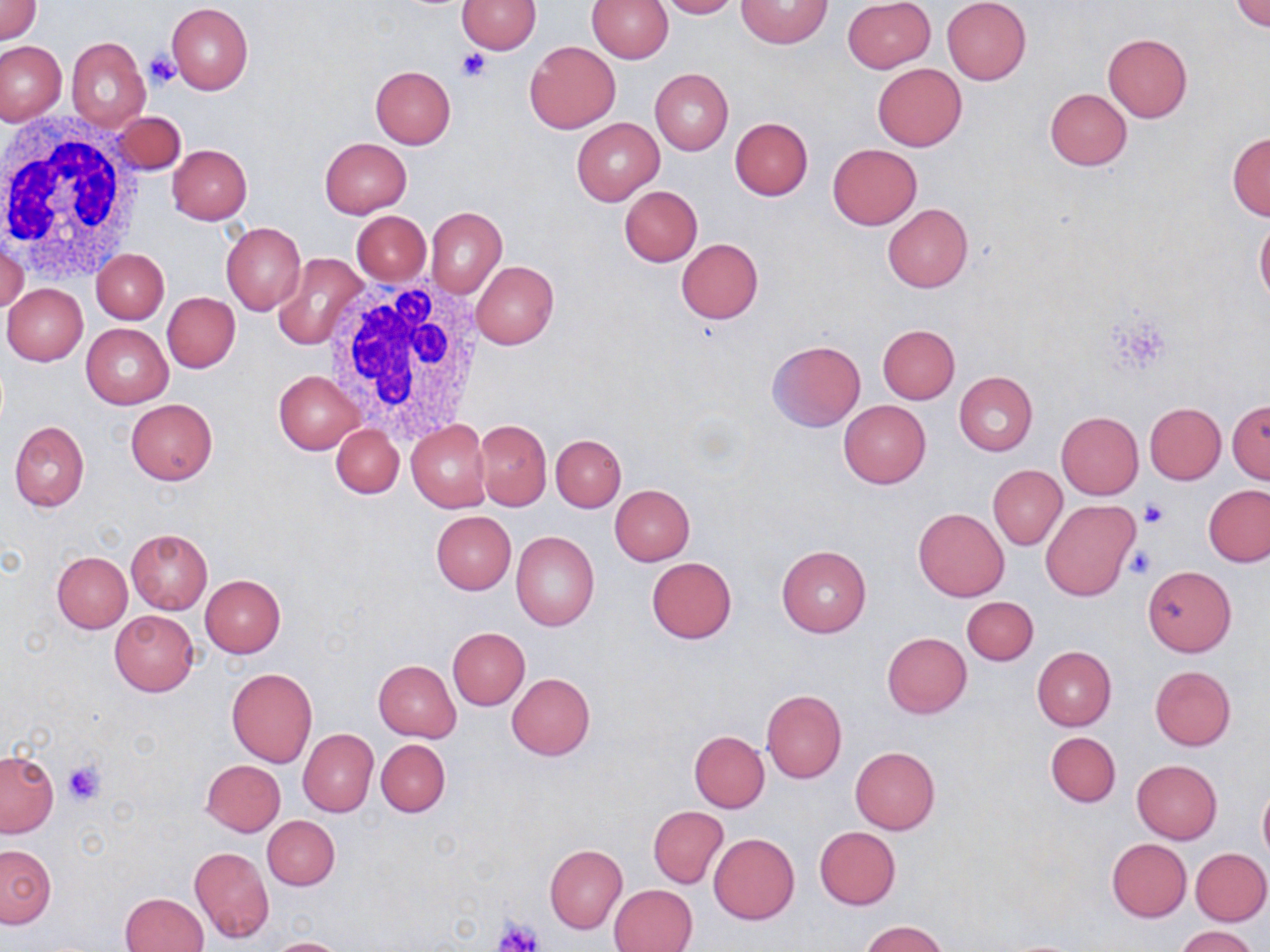
Summary:
  - Coordinate format: approximate bounding boxes as named x1/y1/x2/y2 corners in pixels
  - Uninfected red blood cell locations: (x1=0, y1=0, x2=41, y2=42), (x1=457, y1=0, x2=541, y2=54), (x1=587, y1=0, x2=673, y2=63), (x1=657, y1=0, x2=738, y2=18), (x1=736, y1=0, x2=832, y2=48), (x1=843, y1=0, x2=935, y2=72), (x1=943, y1=0, x2=1032, y2=85), (x1=1233, y1=0, x2=1270, y2=33), (x1=167, y1=2, x2=253, y2=94), (x1=1103, y1=32, x2=1192, y2=121), (x1=67, y1=37, x2=149, y2=130), (x1=0, y1=40, x2=65, y2=124), (x1=525, y1=40, x2=620, y2=134), (x1=873, y1=63, x2=967, y2=150), (x1=371, y1=66, x2=456, y2=148), (x1=650, y1=68, x2=733, y2=155), (x1=1045, y1=89, x2=1131, y2=171), (x1=113, y1=111, x2=185, y2=175), (x1=572, y1=117, x2=664, y2=205), (x1=730, y1=117, x2=813, y2=199), (x1=1227, y1=133, x2=1270, y2=220), (x1=320, y1=137, x2=411, y2=217), (x1=828, y1=143, x2=922, y2=230), (x1=169, y1=145, x2=252, y2=224), (x1=621, y1=186, x2=702, y2=266), (x1=882, y1=203, x2=973, y2=293), (x1=425, y1=206, x2=507, y2=298), (x1=353, y1=211, x2=430, y2=285), (x1=1255, y1=215, x2=1270, y2=304), (x1=222, y1=222, x2=305, y2=316), (x1=1, y1=237, x2=29, y2=317), (x1=676, y1=238, x2=763, y2=323), (x1=93, y1=249, x2=169, y2=323), (x1=274, y1=252, x2=368, y2=351), (x1=471, y1=260, x2=558, y2=349), (x1=3, y1=283, x2=87, y2=366), (x1=162, y1=292, x2=240, y2=373), (x1=82, y1=324, x2=172, y2=408), (x1=877, y1=324, x2=960, y2=404), (x1=767, y1=340, x2=866, y2=431), (x1=274, y1=370, x2=365, y2=453), (x1=954, y1=371, x2=1037, y2=455), (x1=126, y1=400, x2=217, y2=484), (x1=838, y1=401, x2=931, y2=488), (x1=1228, y1=401, x2=1270, y2=484), (x1=1145, y1=403, x2=1225, y2=484), (x1=1056, y1=412, x2=1143, y2=499), (x1=474, y1=419, x2=551, y2=510), (x1=10, y1=420, x2=89, y2=512), (x1=407, y1=420, x2=490, y2=511), (x1=331, y1=423, x2=404, y2=499), (x1=552, y1=434, x2=626, y2=511), (x1=989, y1=466, x2=1066, y2=549), (x1=609, y1=484, x2=695, y2=565), (x1=1203, y1=485, x2=1270, y2=566), (x1=1042, y1=499, x2=1140, y2=602), (x1=913, y1=508, x2=1009, y2=602), (x1=431, y1=511, x2=515, y2=594), (x1=126, y1=529, x2=212, y2=613), (x1=511, y1=531, x2=601, y2=631), (x1=776, y1=545, x2=871, y2=637), (x1=52, y1=551, x2=131, y2=632), (x1=646, y1=557, x2=738, y2=643), (x1=1144, y1=564, x2=1236, y2=655), (x1=200, y1=574, x2=286, y2=657), (x1=963, y1=596, x2=1038, y2=664), (x1=109, y1=611, x2=199, y2=695), (x1=448, y1=627, x2=529, y2=709), (x1=881, y1=632, x2=971, y2=717), (x1=1032, y1=646, x2=1116, y2=730), (x1=373, y1=660, x2=460, y2=742), (x1=1150, y1=666, x2=1237, y2=750), (x1=227, y1=667, x2=317, y2=767), (x1=506, y1=673, x2=595, y2=761), (x1=761, y1=689, x2=847, y2=782), (x1=298, y1=729, x2=378, y2=817), (x1=689, y1=731, x2=770, y2=813), (x1=1045, y1=731, x2=1119, y2=807), (x1=376, y1=739, x2=449, y2=817), (x1=850, y1=746, x2=940, y2=833), (x1=0, y1=750, x2=57, y2=837), (x1=201, y1=759, x2=285, y2=835), (x1=1132, y1=760, x2=1222, y2=844), (x1=1258, y1=780, x2=1270, y2=866), (x1=648, y1=806, x2=727, y2=888), (x1=262, y1=816, x2=339, y2=890), (x1=814, y1=826, x2=901, y2=909), (x1=709, y1=832, x2=799, y2=924), (x1=1106, y1=838, x2=1191, y2=921), (x1=0, y1=845, x2=55, y2=927), (x1=545, y1=845, x2=626, y2=932), (x1=190, y1=846, x2=274, y2=942), (x1=1190, y1=847, x2=1270, y2=924), (x1=611, y1=884, x2=697, y2=952), (x1=120, y1=892, x2=208, y2=952), (x1=862, y1=921, x2=947, y2=952), (x1=1175, y1=926, x2=1258, y2=952), (x1=264, y1=937, x2=352, y2=952)
  - Platelet locations: (x1=456, y1=46, x2=490, y2=82), (x1=144, y1=53, x2=180, y2=90), (x1=1141, y1=499, x2=1170, y2=529), (x1=1124, y1=547, x2=1157, y2=579), (x1=64, y1=759, x2=104, y2=806), (x1=497, y1=917, x2=544, y2=950)
  - White blood cell locations: (x1=0, y1=118, x2=149, y2=283), (x1=321, y1=275, x2=491, y2=444)
  - Slide-level diagnosis: no evidence of blood parasites
  - Modality: optical microscopy
  - Preparation: thin blood smear
  - Magnification: 1000x
  - Field of view: one of a larger specimen
  - Image size: 1270×952 pixels
  - Stain: May-Grünwald-Giemsa